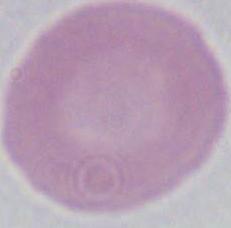 1000x magnification. A red blood cell is seen. Micrograph.